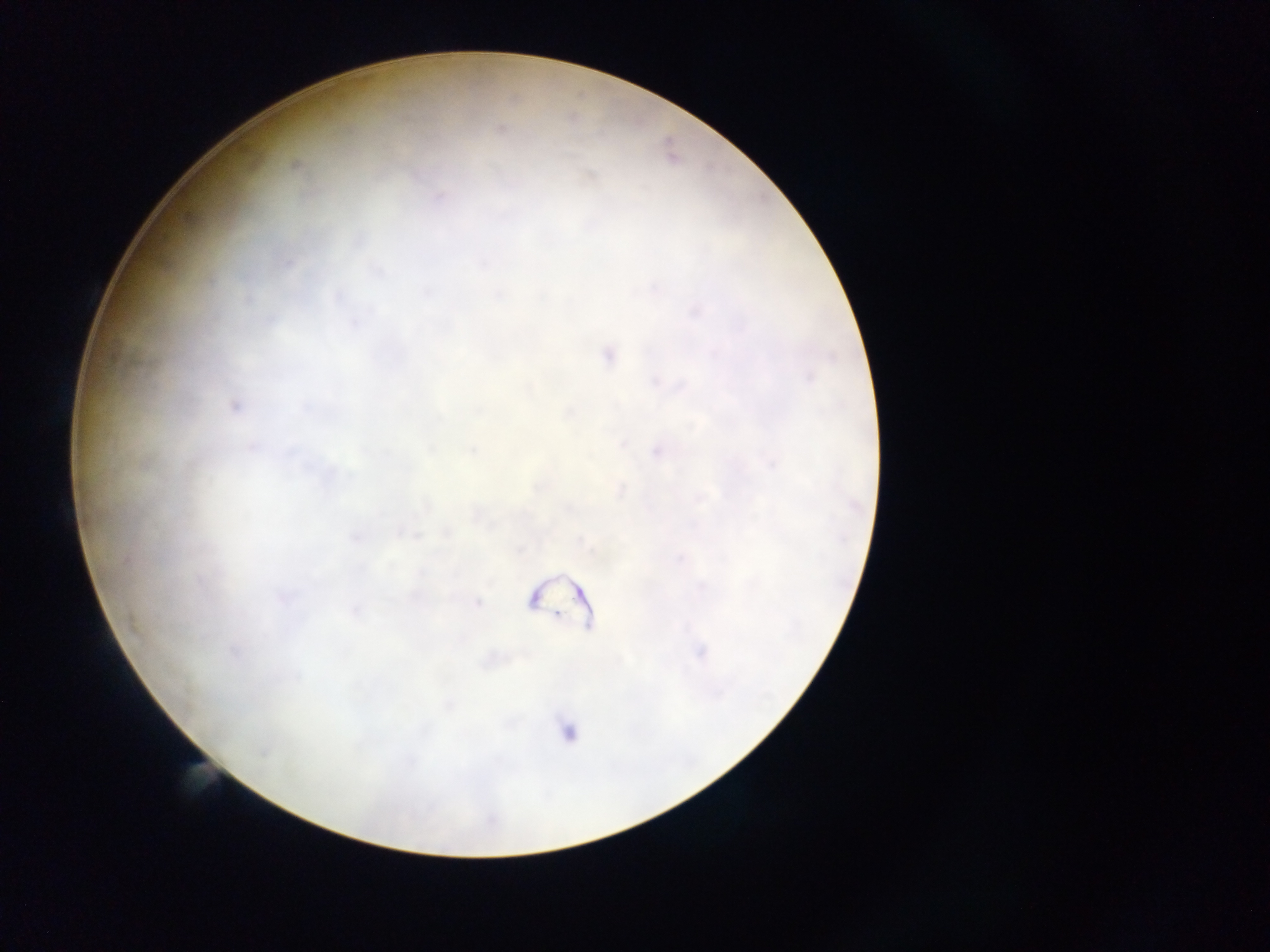

Plasmodium parasite locations = approximate centers as (x, y) in pixels: (501, 128), (440, 197), (287, 263), (378, 269), (427, 293), (338, 296), (353, 323), (607, 354), (234, 406), (622, 444), (473, 451), (655, 451), (772, 464), (446, 533), (412, 534), (356, 538), (127, 561), (282, 598), (477, 603), (132, 625), (235, 652), (701, 652), (567, 732)
preparation = thick blood smear
field of view = single
image size = 1270×952 pixels
country = Ghana
capture = mobile-phone photograph through a microscope